Report the malaria status.
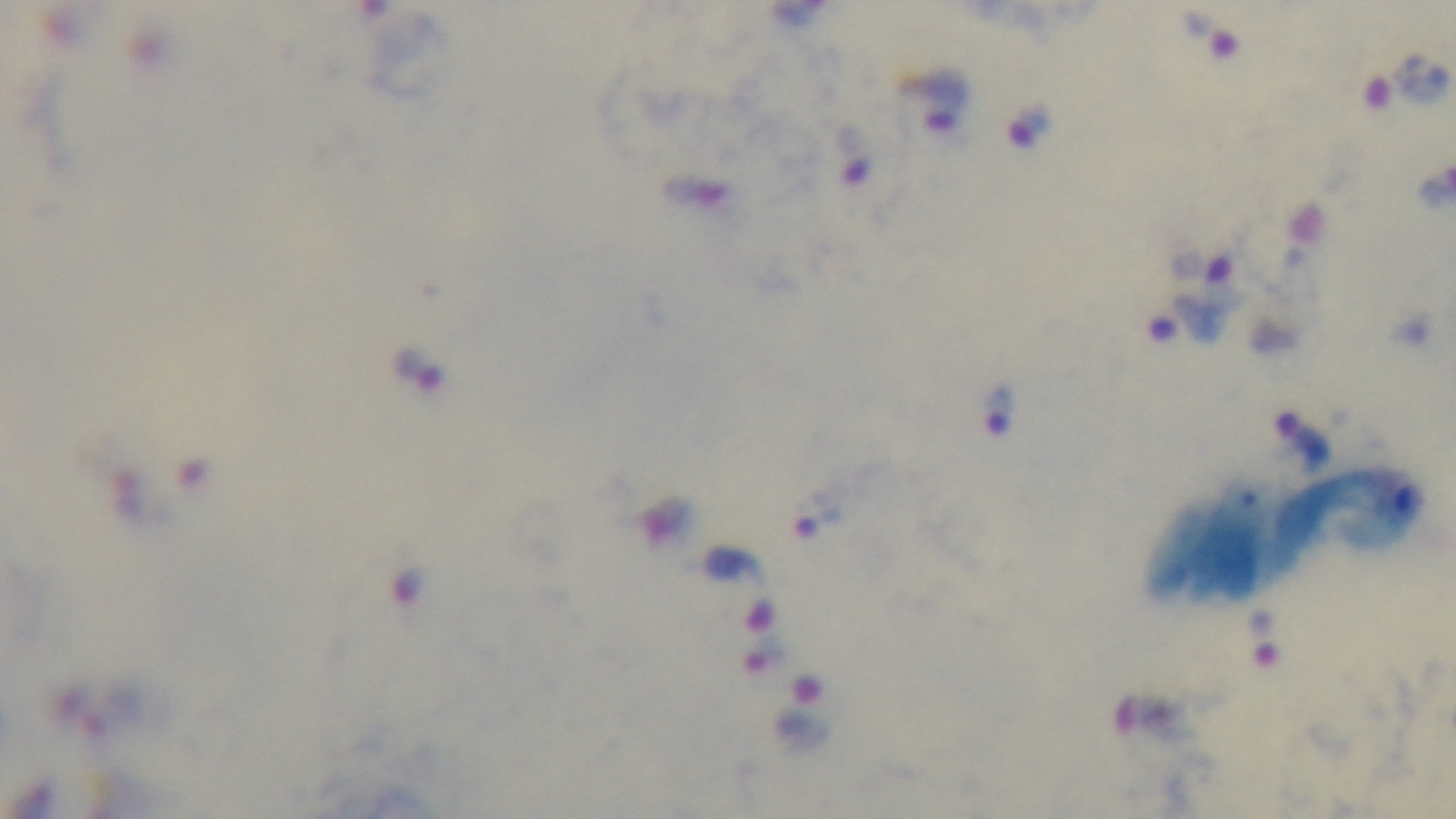

It is infected.

Oil-immersion objective, 100x. Preparation: thick smear. Giemsa stain. Captured with a mounted 4K digital camera. Single field of view. Light microscopy.